Assess this cell for malaria.
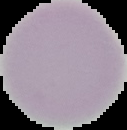

It is uninfected.

preparation = thin blood smear
image size = 127×130 pixels
image type = cell region segmented out of the field of view; surrounding area masked to black